Name the parasite shown.
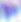

This is Toxoplasma gondii.

Summary:
  - Magnification: 400x
  - Modality: micrograph